Report the malaria status of this cell.
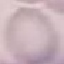
It is uninfected.

preparation = thin blood film
capture = smartphone camera at the microscope eyepiece
stain = Giemsa
image type = cell patch, automatically extracted from a larger field of view and resized to 64 × 64 pixels